Point out each malaria parasite.
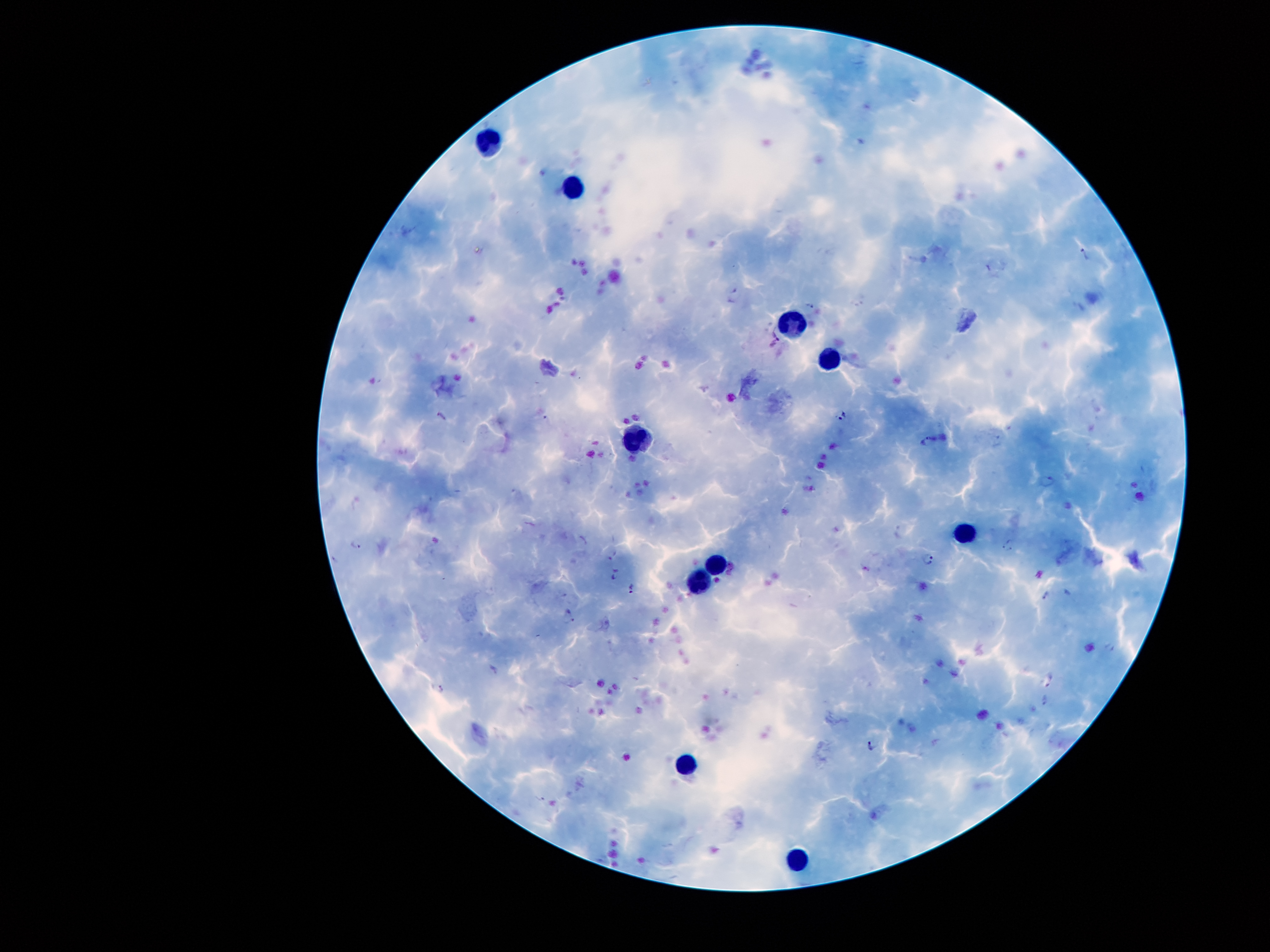
Approximate centers as [x, y] in pixels.
Malaria parasites: [1084, 255], [737, 292], [810, 306], [776, 336], [842, 414], [442, 418], [928, 440], [1046, 480], [1008, 544], [355, 546], [928, 558], [613, 572], [632, 590], [1045, 596], [568, 618], [1110, 648], [493, 669], [1050, 679], [439, 688], [1045, 700], [871, 744].

Summary:
  - Leukocyte locations: [491, 139], [576, 185], [789, 319], [831, 354], [640, 438], [963, 531], [717, 561], [697, 582], [685, 766], [793, 855]
  - Magnification: 100x
  - Capture: smartphone camera through the microscope eyepiece
  - Preparation: thick peripheral-blood smear
  - Stain: Giemsa
  - Patient malaria status: positive for Plasmodium falciparum
  - Image size: 1270×952 pixels
  - Field of view: one from this slide